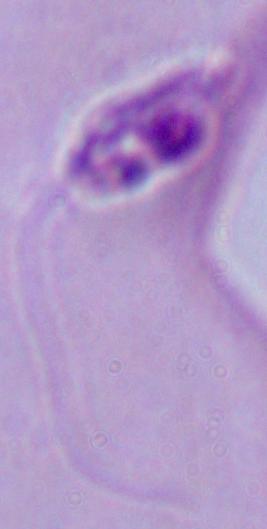
Micrograph. A Leishmania parasite is shown. 1000x magnification.